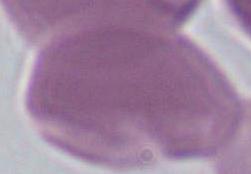
Summary:
  - Modality: photomicrograph
  - Identification: Plasmodium
  - Magnification: 400x or 1000x